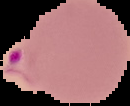
Summary:
  - Image type: segmented cell region on a black background
  - Malaria status: parasitized
  - Image size: 130×106 pixels
  - Preparation: thin blood smear